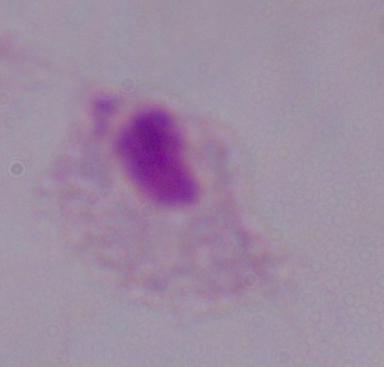

modality = photomicrograph
identification = trichomonad
magnification = 1000x